Locate every malaria parasite.
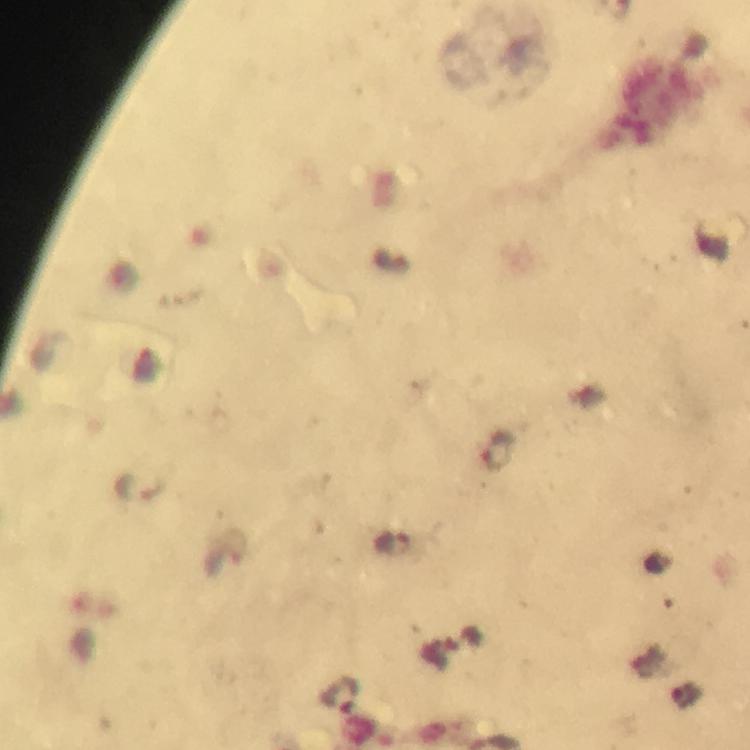
Approximate centers as [x, y] in pixels.
Malaria parasites: [499, 453], [139, 489], [390, 545], [225, 555], [340, 694].

Summary:
  - Cropped from: one field of view
  - Immersion oil: applied
  - Image size: 750×750 pixels
  - Preparation: thick blood smear
  - Stain: Giemsa
  - Context: from a malaria diagnostic workup
  - Capture: smartphone mounted on the microscope
  - Magnification: 100x